Classify this cell by malaria status.
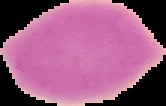

It is uninfected.

Cell region segmented out of the field of view; the surrounding area is masked to black. Image is 166×106 pixels. From a thin blood film.